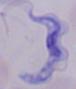

A trypanosome is shown. 1000x magnification. Micrograph.